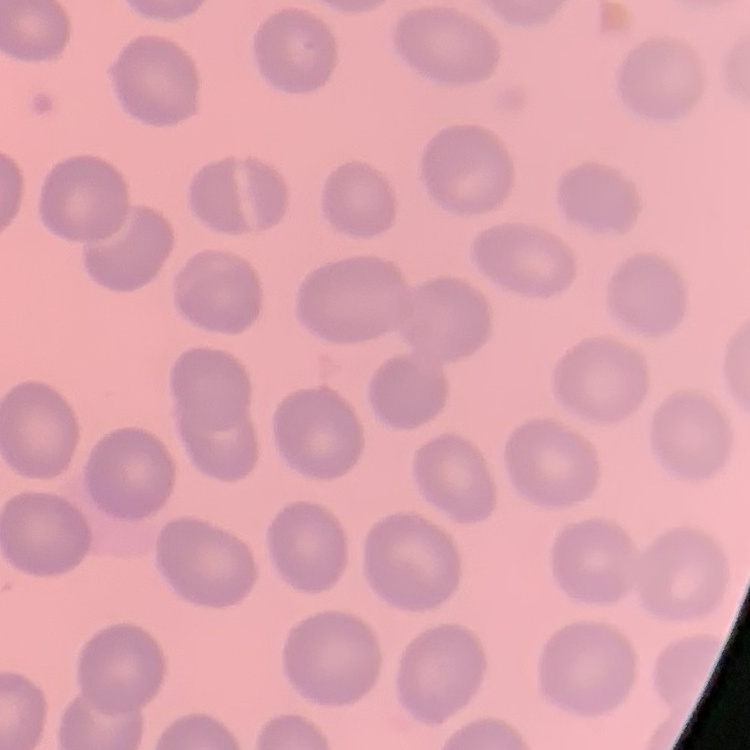

erythrocyte morphology = no rouleaux formation
preparation = thin blood film
stain = Field's or Giemsa
image type = square crop of a larger photomicrograph